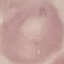

Summary:
  - Malaria status: uninfected
  - Preparation: thin blood film
  - Stain: Giemsa
  - Image type: automatically extracted cell patch, resized to 64 × 64 pixels
  - Capture: smartphone camera at the microscope eyepiece